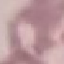
Summary:
  - Malaria status: uninfected
  - Preparation: thin blood smear
  - Image type: automatically extracted cell patch, resized to 64 × 64 pixels
  - Stain: Giemsa
  - Capture: smartphone camera at the microscope eyepiece